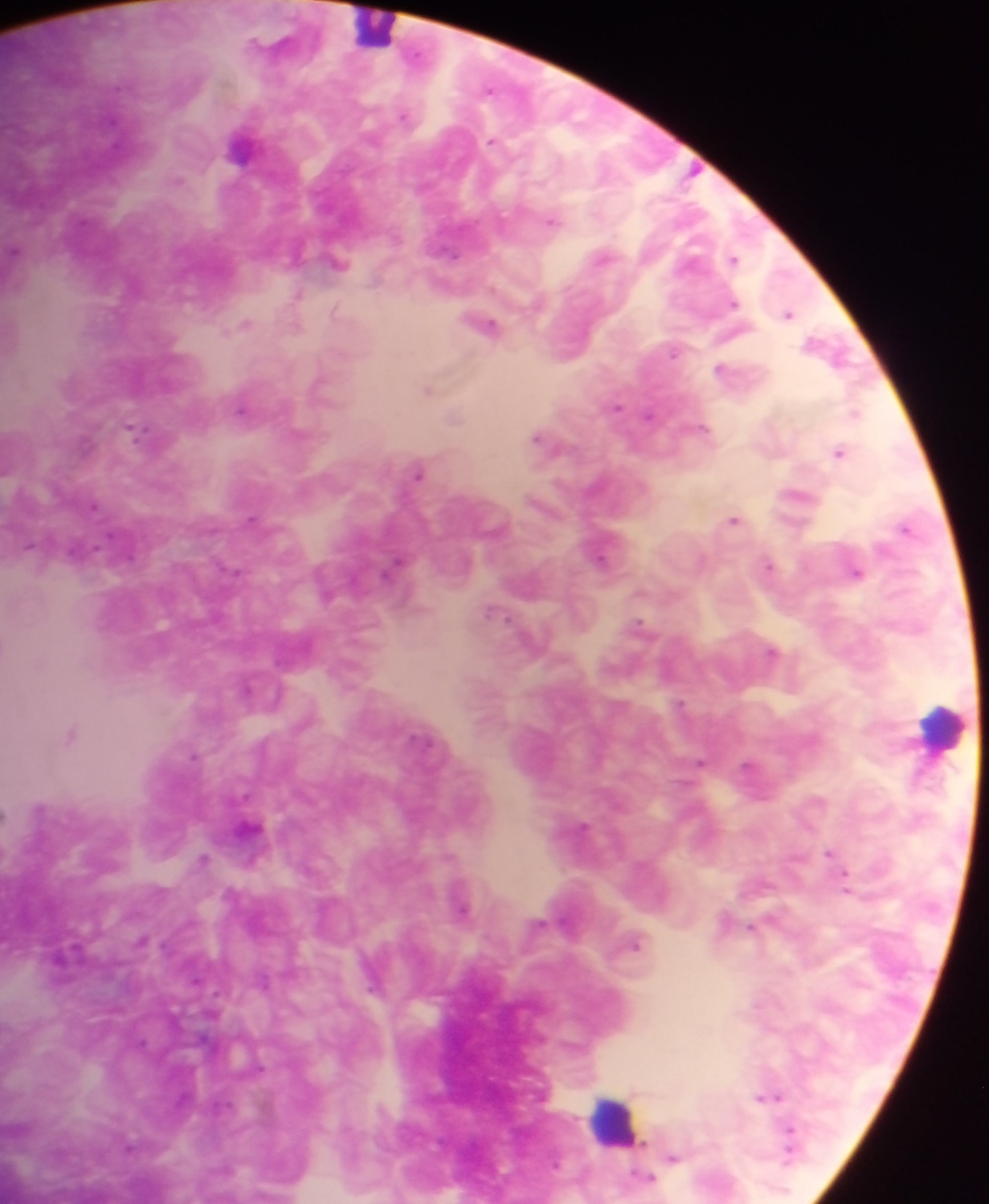

Approximate centers as [x, y] in pixels.
Summary:
  - Leukocyte locations: [374, 26], [940, 726], [613, 1118]
  - Plasmodium parasite locations: [404, 115], [491, 141], [552, 221], [14, 252], [454, 256], [734, 259], [297, 295], [734, 304], [789, 314], [487, 324], [245, 325], [673, 353], [720, 368], [428, 389], [616, 407], [241, 409], [855, 413], [648, 415], [703, 427], [134, 429], [537, 437], [839, 452], [419, 473], [95, 507], [251, 518], [734, 520], [906, 528], [29, 545], [600, 557], [394, 564], [768, 565], [856, 573], [491, 612], [639, 623], [772, 652], [681, 703], [72, 734], [194, 755], [699, 762], [748, 765], [583, 827], [830, 853], [203, 859], [847, 886], [462, 906], [752, 928], [635, 945], [778, 1096], [762, 1098], [789, 1133], [789, 1152], [672, 1157], [649, 1177]
  - Image size: 989×1204 pixels
  - Country: Ghana
  - Field of view: single
  - Capture: mobile-phone photograph through a microscope
  - Preparation: thick blood smear